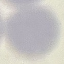

malaria status = uninfected
capture = smartphone camera at the microscope eyepiece
image type = cell patch, automatically extracted from a larger field of view and resized to 64 × 64 pixels
preparation = thin smear
stain = Giemsa